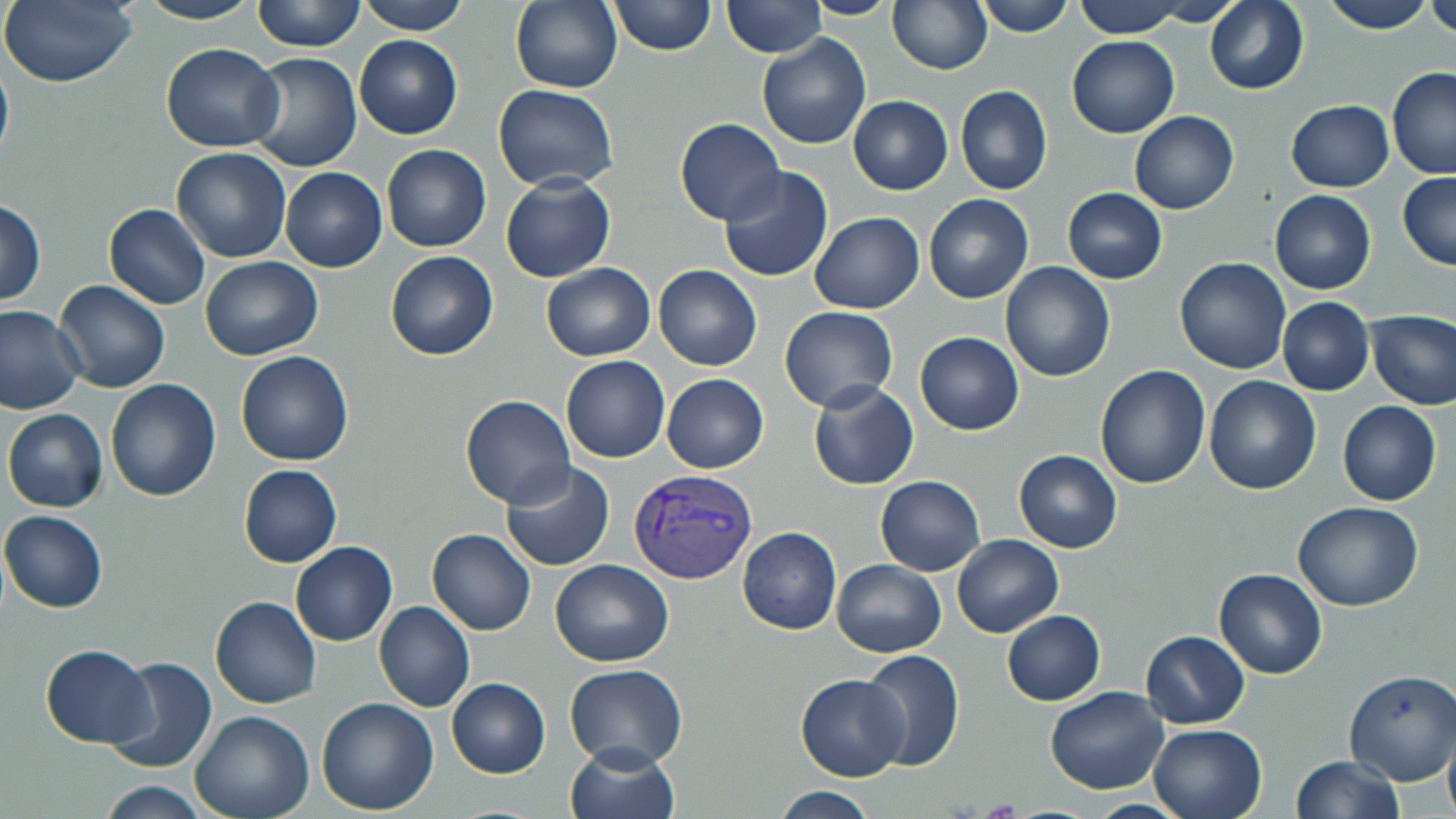

Approximate bounding boxes as named x1/y1/x2/y2 corners in pixels. Uninfected red blood cell locations: (x1=0, y1=0, x2=137, y2=88), (x1=252, y1=0, x2=365, y2=51), (x1=354, y1=0, x2=468, y2=35), (x1=607, y1=0, x2=715, y2=56), (x1=721, y1=0, x2=826, y2=58), (x1=802, y1=0, x2=900, y2=20), (x1=972, y1=0, x2=1075, y2=37), (x1=1071, y1=0, x2=1190, y2=38), (x1=1205, y1=0, x2=1308, y2=94), (x1=1318, y1=0, x2=1436, y2=34), (x1=137, y1=1, x2=263, y2=24), (x1=510, y1=1, x2=622, y2=93), (x1=876, y1=1, x2=979, y2=140), (x1=887, y1=1, x2=993, y2=74), (x1=1138, y1=1, x2=1246, y2=26), (x1=1424, y1=2, x2=1456, y2=38), (x1=756, y1=33, x2=871, y2=149), (x1=354, y1=35, x2=462, y2=140), (x1=1068, y1=36, x2=1179, y2=138), (x1=160, y1=44, x2=285, y2=151), (x1=0, y1=49, x2=14, y2=171), (x1=247, y1=53, x2=362, y2=172), (x1=1386, y1=67, x2=1456, y2=179), (x1=494, y1=85, x2=618, y2=191), (x1=955, y1=85, x2=1052, y2=196), (x1=848, y1=95, x2=953, y2=195), (x1=1285, y1=100, x2=1395, y2=193), (x1=1129, y1=111, x2=1239, y2=215), (x1=675, y1=117, x2=784, y2=224), (x1=381, y1=143, x2=491, y2=252), (x1=171, y1=147, x2=292, y2=262), (x1=280, y1=167, x2=387, y2=272), (x1=717, y1=167, x2=834, y2=282), (x1=1398, y1=173, x2=1456, y2=270), (x1=499, y1=174, x2=615, y2=284), (x1=1061, y1=187, x2=1167, y2=284), (x1=1269, y1=191, x2=1376, y2=294), (x1=923, y1=195, x2=1034, y2=304), (x1=1, y1=198, x2=46, y2=305), (x1=104, y1=204, x2=210, y2=309), (x1=809, y1=211, x2=924, y2=313), (x1=385, y1=250, x2=498, y2=361), (x1=200, y1=255, x2=323, y2=361), (x1=1175, y1=256, x2=1291, y2=374), (x1=1002, y1=261, x2=1116, y2=382), (x1=540, y1=263, x2=655, y2=361), (x1=654, y1=264, x2=762, y2=371), (x1=53, y1=279, x2=169, y2=392), (x1=1276, y1=298, x2=1374, y2=396), (x1=0, y1=306, x2=85, y2=416), (x1=779, y1=306, x2=898, y2=412), (x1=1365, y1=310, x2=1455, y2=410), (x1=914, y1=332, x2=1024, y2=435), (x1=235, y1=350, x2=353, y2=467), (x1=560, y1=355, x2=670, y2=462), (x1=1093, y1=364, x2=1210, y2=490), (x1=662, y1=374, x2=767, y2=474), (x1=1204, y1=374, x2=1320, y2=494), (x1=105, y1=378, x2=222, y2=501), (x1=808, y1=380, x2=919, y2=490), (x1=460, y1=394, x2=576, y2=508), (x1=1337, y1=401, x2=1441, y2=506), (x1=3, y1=408, x2=107, y2=512), (x1=1014, y1=450, x2=1122, y2=552), (x1=499, y1=461, x2=616, y2=572), (x1=238, y1=464, x2=342, y2=567), (x1=875, y1=475, x2=985, y2=575), (x1=1294, y1=502, x2=1423, y2=612), (x1=1, y1=509, x2=107, y2=613), (x1=737, y1=526, x2=842, y2=635), (x1=427, y1=529, x2=536, y2=636), (x1=951, y1=534, x2=1063, y2=638), (x1=291, y1=541, x2=397, y2=647), (x1=830, y1=559, x2=946, y2=657), (x1=550, y1=560, x2=674, y2=667), (x1=1213, y1=568, x2=1327, y2=679), (x1=211, y1=596, x2=320, y2=708), (x1=373, y1=601, x2=475, y2=712), (x1=1002, y1=611, x2=1106, y2=706), (x1=1140, y1=630, x2=1251, y2=728), (x1=39, y1=644, x2=155, y2=748), (x1=859, y1=649, x2=965, y2=772), (x1=106, y1=657, x2=217, y2=774), (x1=564, y1=663, x2=689, y2=768), (x1=1342, y1=670, x2=1456, y2=785), (x1=795, y1=674, x2=909, y2=782), (x1=446, y1=678, x2=550, y2=778), (x1=1045, y1=687, x2=1169, y2=794), (x1=316, y1=697, x2=439, y2=814), (x1=189, y1=711, x2=313, y2=819), (x1=1148, y1=722, x2=1268, y2=819), (x1=1443, y1=734, x2=1456, y2=819), (x1=565, y1=743, x2=681, y2=819), (x1=1292, y1=755, x2=1405, y2=819), (x1=97, y1=782, x2=211, y2=817), (x1=771, y1=786, x2=877, y2=818). Plasmodium vivax-infected red blood cell locations: (x1=629, y1=469, x2=758, y2=585). Slide-level diagnosis: Plasmodium vivax. Image is 1456×819 pixels. Captured at 1000x magnification. Single field of view. Thin blood smear. May-Grünwald-Giemsa-stained preparation. Light microscopy.